Locate every Plasmodium parasite.
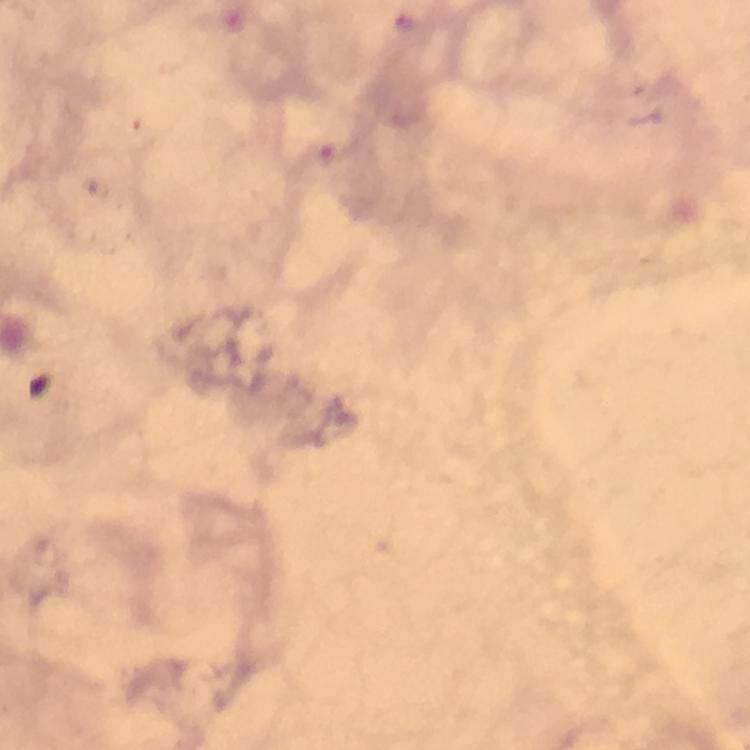
Approximate centers as {x, y} in pixels.
Plasmodium parasites: {404, 21}, {329, 154}.

Image is 750×750 pixels. Thick smear. Giemsa stain. From a diagnostic examination for malaria. Smartphone photograph taken through a microscope. Immersion oil applied. Cropped region of a single field of view. 100x magnification.